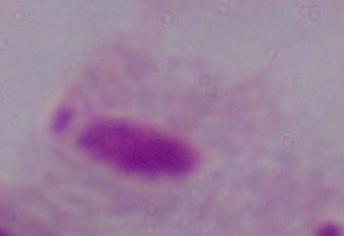

1000x magnification. Micrograph. A trichomonad is shown.